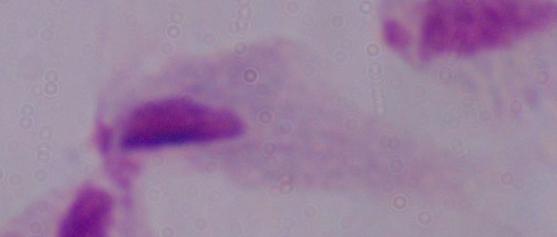

identification = trichomonad
magnification = 1000x
modality = micrograph